Locate every leukocyte (white blood cell).
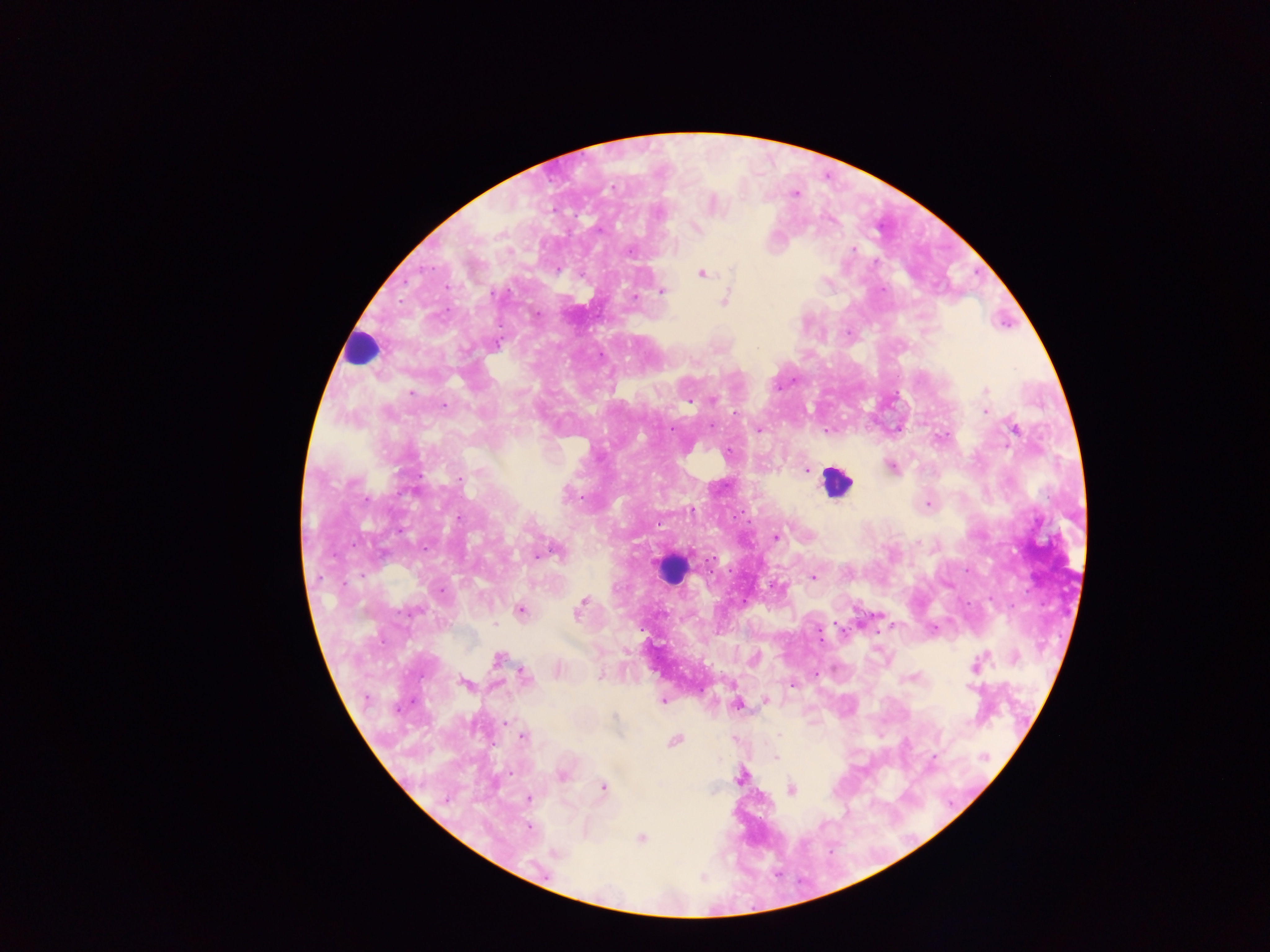
Approximate centers as {x, y} in pixels.
Leukocytes: {361, 347}, {836, 481}, {671, 568}.

{
  "field_of_view": "single",
  "preparation": "thick blood smear",
  "capture": "mobile-phone photograph through a microscope",
  "country": "Ghana",
  "malaria_parasite_locations": "approximate centers as {x, y} in pixels: {795, 194}, {658, 214}, {695, 229}, {630, 252}, {732, 270}, {702, 274}, {662, 291}, {493, 294}, {633, 296}, {725, 301}, {537, 314}, {498, 343}, {985, 390}, {410, 394}, {714, 401}, {687, 402}, {985, 402}, {443, 405}, {986, 412}, {711, 426}, {1014, 429}, {671, 430}, {760, 430}, {728, 453}, {891, 467}, {807, 470}, {459, 479}, {566, 496}, {580, 497}, {928, 505}, {691, 509}, {460, 518}, {776, 537}, {557, 553}, {538, 556}, {813, 577}, {442, 590}, {581, 603}, {413, 611}, {521, 611}, {578, 613}, {495, 625}, {933, 629}, {497, 658}, {976, 665}, {558, 671}, {524, 675}, {599, 677}, {465, 683}, {793, 685}, {971, 688}, {766, 699}, {662, 700}, {737, 704}, {615, 716}, {506, 723}, {510, 728}, {780, 736}, {522, 737}, {674, 740}, {776, 757}, {934, 757}, {985, 757}, {561, 775}, {739, 777}, {603, 787}, {791, 789}, {529, 799}, {445, 800}, {529, 828}, {641, 839}, {557, 853}",
  "image_size": "1270×952 pixels"
}